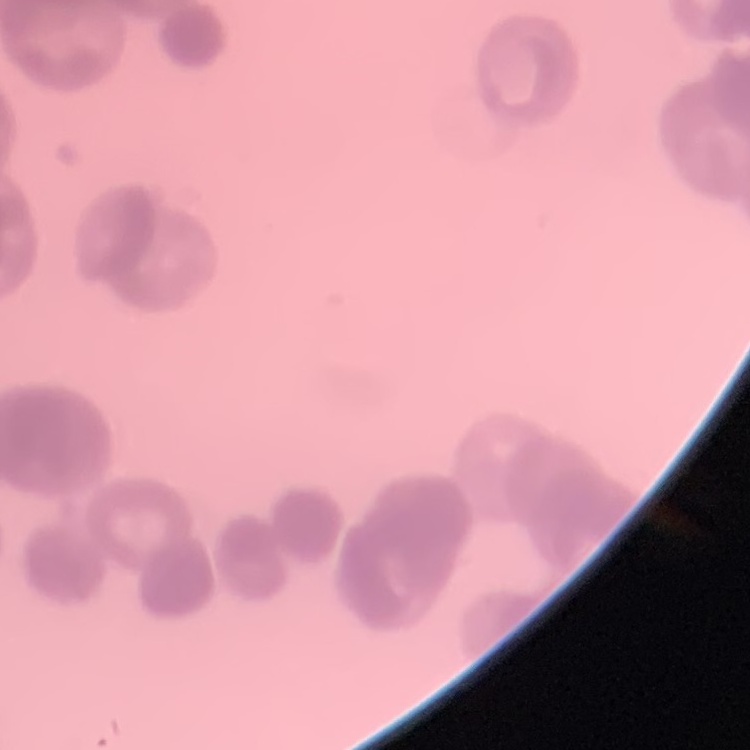 The red blood cells exhibit rouleaux formation. Stained with either Field's or Giemsa. Thin blood film. One tile cut from a larger photomicrograph.